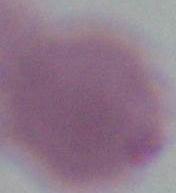

identification: red blood cell
modality: photomicrograph
magnification: 1000x